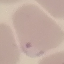

Malaria status: parasitized. Thin blood film. Automatically extracted cell patch, resized to 64 × 64 pixels. Giemsa stain. Acquired by smartphone through the microscope eyepiece.